Locate every blood parasite and identify its species.
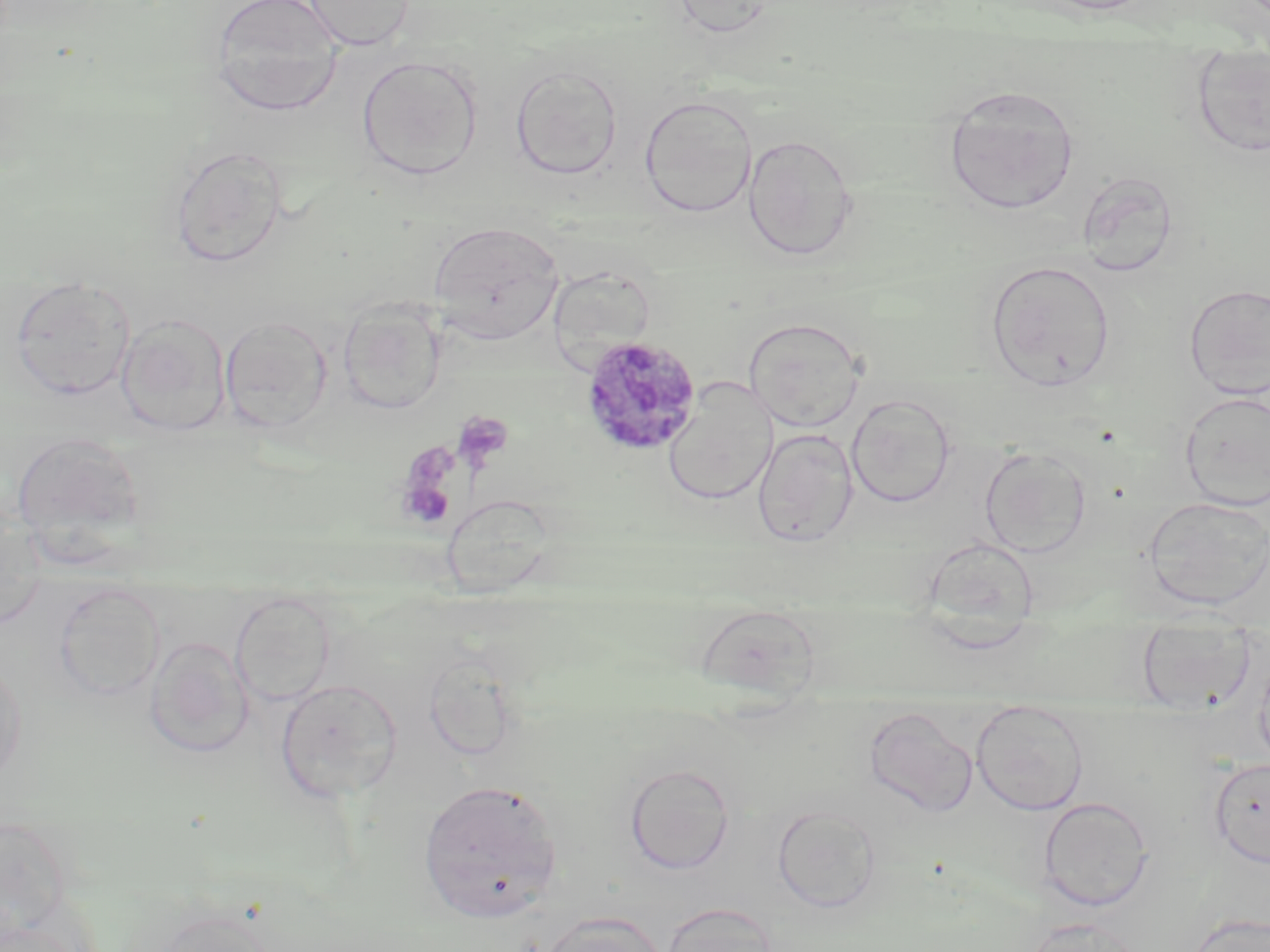

Approximate bounding boxes as (x1, y1, x2, y2) in pixels.
Plasmodium malariae-infected red blood cells: (579, 334, 703, 457).
No Plasmodium falciparum, Plasmodium ovale, Plasmodium vivax, Babesia divergens, or Trypanosoma brucei observed.

slide-level diagnosis = Plasmodium malariae
image size = 1270×952 pixels
preparation = thin blood film
magnification = 1000x
uninfected red blood cell locations = approximate bounding boxes as (x1, y1, x2, y2) in pixels: (210, 0, 344, 115), (303, 0, 415, 51), (669, 0, 780, 39), (1190, 48, 1270, 158), (357, 54, 484, 181), (510, 65, 622, 180), (943, 85, 1079, 215), (639, 94, 758, 217), (743, 133, 859, 260), (168, 144, 289, 267), (428, 221, 563, 343), (985, 259, 1115, 391), (10, 275, 136, 400), (1183, 283, 1270, 400), (337, 298, 447, 414), (116, 313, 232, 436), (219, 315, 334, 433), (743, 317, 866, 432), (663, 380, 777, 506), (1180, 390, 1270, 511), (846, 394, 955, 508), (752, 428, 859, 547), (10, 430, 146, 552), (978, 446, 1092, 558), (443, 493, 554, 599), (1143, 496, 1270, 610), (0, 504, 46, 631), (922, 537, 1040, 646), (53, 582, 165, 701), (229, 591, 336, 707), (695, 603, 821, 702), (1136, 621, 1258, 712), (145, 636, 255, 758), (423, 651, 521, 762), (0, 656, 27, 789), (276, 678, 403, 802), (971, 700, 1089, 815), (864, 705, 977, 817), (1209, 757, 1270, 868), (623, 762, 736, 875), (416, 778, 563, 922), (1039, 796, 1154, 911), (773, 804, 882, 914), (661, 901, 779, 952), (141, 904, 283, 952), (535, 910, 668, 952), (1184, 912, 1269, 952), (1023, 917, 1144, 952), (0, 918, 89, 952)
platelet locations = approximate bounding boxes as (x1, y1, x2, y2) in pixels: (452, 410, 514, 473), (397, 461, 457, 530)
field of view = single
modality = optical microscopy
stain = May-Grünwald-Giemsa